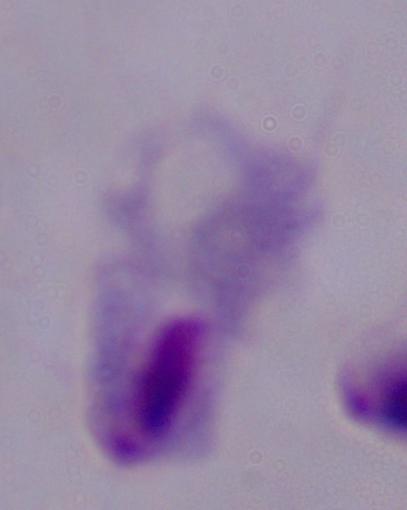
Summary:
  - Magnification: 1000x
  - Modality: photomicrograph
  - Identification: trichomonad